Classify this cell by malaria status.
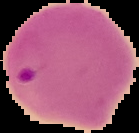

Parasitized.

From a thin blood smear. Cell region segmented out of the field of view; the surrounding area is masked to black. Image is 139×133 pixels.